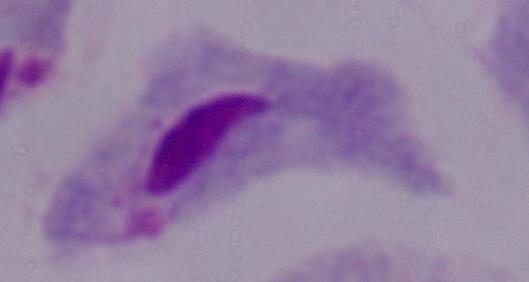
Summary:
  - Magnification: 1000x
  - Identification: trichomonad
  - Modality: micrograph